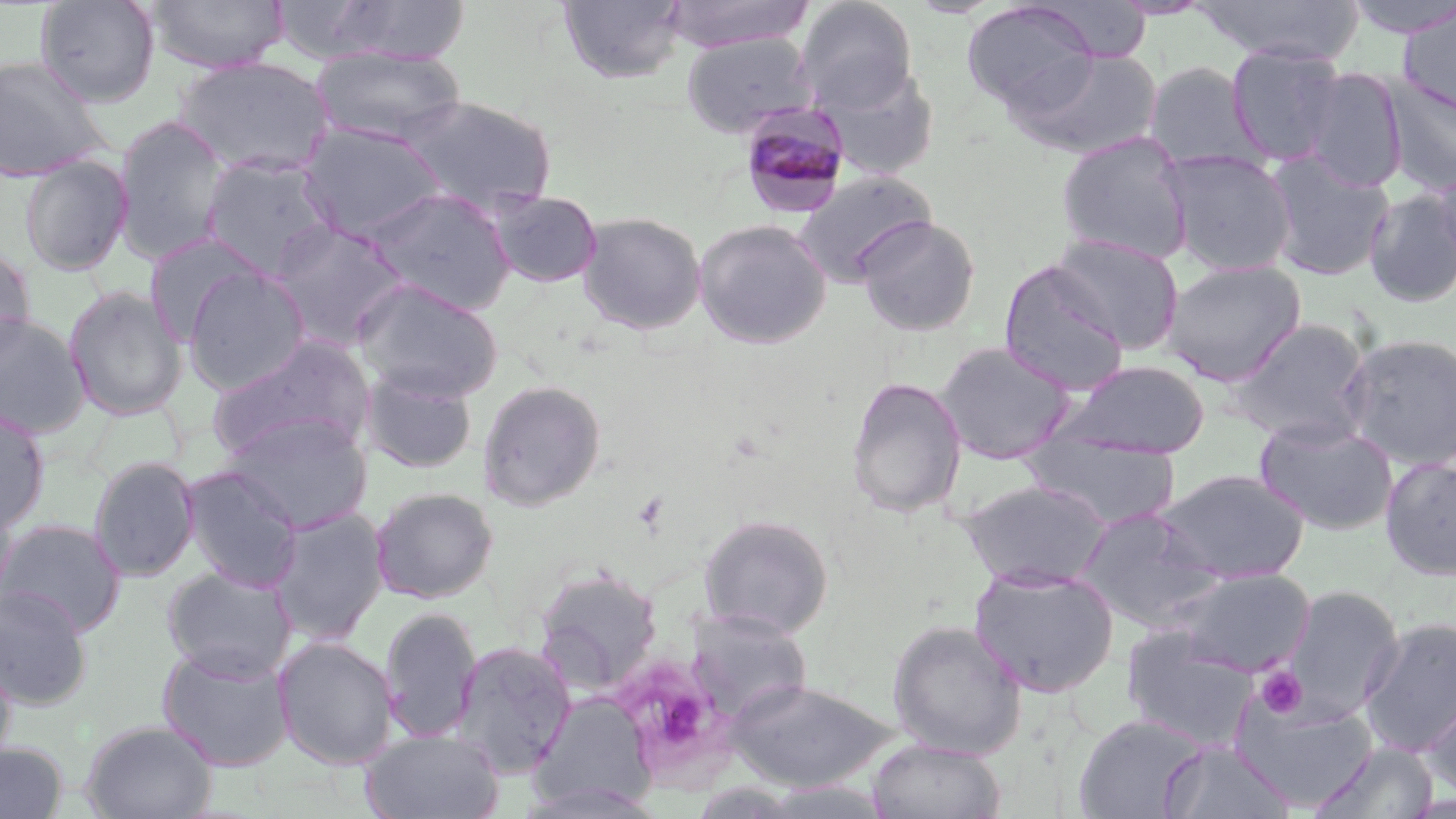
Summary:
  - Coordinate format: approximate bounding boxes as (x1, y1, x2, y2) in pixels
  - Plasmodium malariae-infected red blood cell locations: (737, 101, 852, 218)
  - Uninfected red blood cell locations: (146, 0, 289, 74), (557, 0, 688, 85), (662, 0, 816, 53), (795, 0, 918, 113), (1108, 0, 1214, 19), (1194, 0, 1366, 65), (1341, 0, 1456, 39), (34, 1, 160, 108), (323, 1, 474, 64), (961, 1, 1100, 113), (1035, 1, 1153, 63), (1397, 3, 1456, 119), (680, 33, 817, 138), (1226, 43, 1347, 165), (309, 46, 468, 148), (1010, 47, 1162, 160), (0, 55, 109, 182), (173, 56, 333, 177), (1144, 61, 1262, 174), (817, 64, 940, 181), (1301, 67, 1408, 193), (1383, 75, 1456, 198), (401, 95, 557, 217), (112, 114, 232, 264), (298, 121, 448, 242), (1055, 131, 1195, 265), (1162, 150, 1297, 276), (1262, 150, 1395, 282), (199, 154, 338, 280), (19, 156, 132, 275), (1428, 171, 1456, 276), (793, 172, 935, 287), (365, 187, 516, 316), (488, 189, 603, 288), (1363, 189, 1456, 307), (577, 211, 707, 335), (856, 216, 981, 337), (268, 219, 412, 352), (693, 219, 831, 349), (143, 231, 270, 345), (1046, 233, 1185, 354), (0, 245, 36, 359), (1161, 259, 1306, 385), (999, 262, 1130, 395), (182, 265, 311, 395), (352, 278, 504, 402), (63, 285, 187, 421), (0, 312, 92, 439), (1227, 318, 1376, 446), (1340, 332, 1456, 471), (205, 334, 375, 463), (934, 341, 1075, 464), (1061, 359, 1210, 459), (359, 367, 479, 475), (845, 376, 967, 518), (477, 379, 607, 510), (0, 407, 50, 533), (221, 413, 372, 534), (1255, 416, 1397, 535), (1022, 433, 1180, 530), (88, 456, 200, 582), (1379, 456, 1456, 581), (181, 465, 304, 592), (1156, 468, 1310, 583), (959, 479, 1112, 590), (370, 487, 498, 603), (0, 492, 18, 610), (267, 507, 389, 646), (1075, 507, 1223, 629), (698, 513, 834, 638), (0, 517, 126, 637), (161, 566, 296, 682), (534, 566, 662, 695), (969, 566, 1119, 698), (1166, 567, 1316, 676), (0, 585, 93, 710), (1279, 585, 1405, 722), (379, 606, 482, 744), (684, 608, 815, 722), (1359, 616, 1456, 758), (887, 619, 1027, 758), (1121, 625, 1261, 751), (273, 636, 399, 770), (452, 640, 577, 777), (156, 645, 295, 772), (0, 650, 17, 773), (724, 678, 900, 792), (1421, 687, 1456, 802), (531, 694, 657, 811), (1232, 698, 1378, 811), (1072, 714, 1208, 819), (80, 719, 217, 819), (361, 730, 504, 819), (868, 738, 1006, 819), (1158, 739, 1293, 818), (0, 741, 69, 819), (1307, 742, 1439, 818), (759, 781, 894, 818)
  - Platelet locations: (1254, 666, 1307, 719)
  - Slide-level diagnosis: Plasmodium malariae
  - Field of view: one of a larger specimen
  - Magnification: 1000x
  - Image size: 1456×819 pixels
  - Modality: optical microscopy
  - Preparation: thin blood smear
  - Stain: May-Grünwald-Giemsa